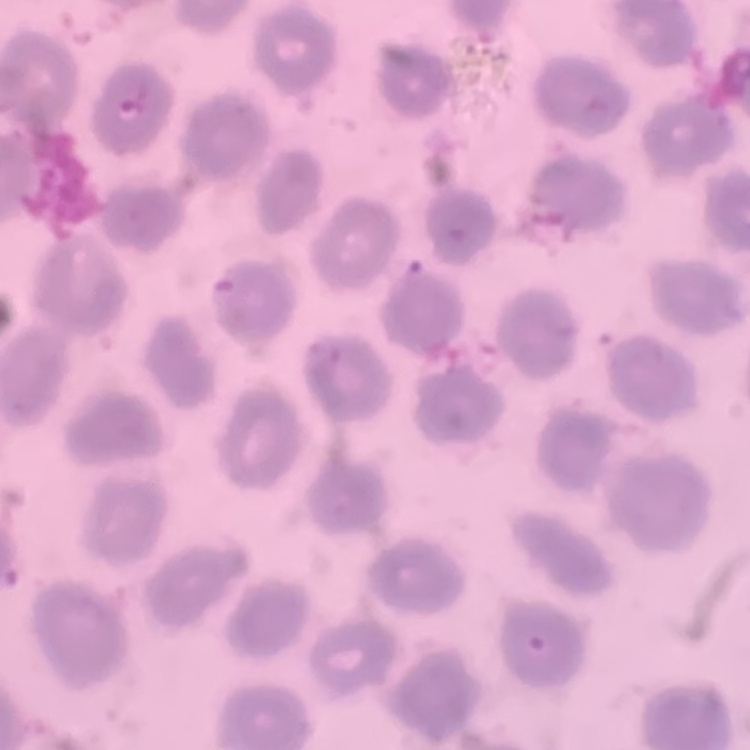

erythrocyte morphology = no rouleaux formation
stain = Field's or Giemsa
preparation = thin peripheral smear
image type = square crop of a larger photomicrograph